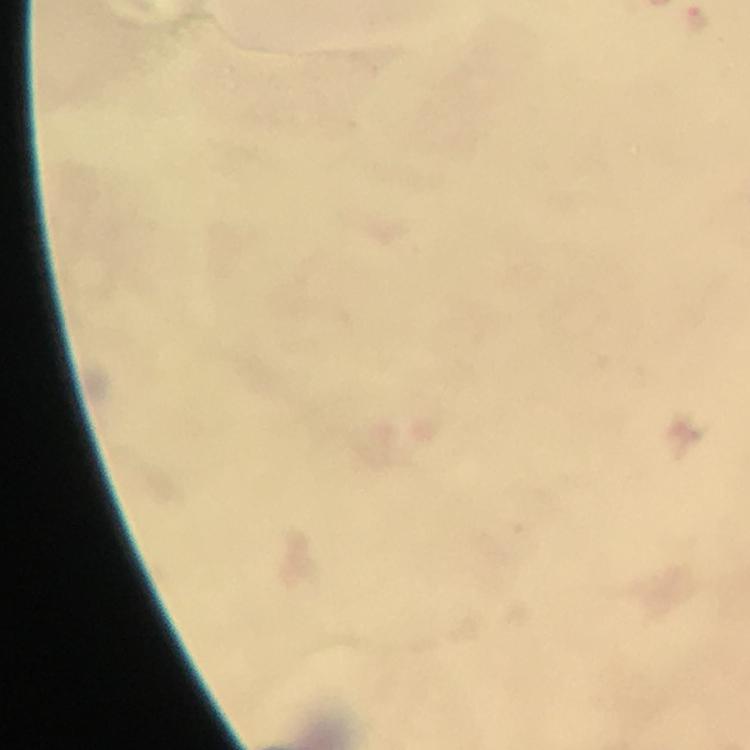

Approximate object centers, in pixels from the top-left corner.
Summary:
  - Plasmodium parasite locations: (x=697, y=17)
  - Context: from a diagnostic examination for malaria
  - Immersion oil: used
  - Preparation: thick blood smear
  - Stain: Giemsa
  - Image size: 750×750 pixels
  - Capture: smartphone photograph through a microscope
  - Magnification: 100x
  - Cropped from: one field of view